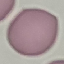
result: negative for malaria parasites
preparation: thin blood film
stain: Giemsa
capture: smartphone through the microscope eyepiece
image_type: cell patch, automatically extracted from a larger field of view and resized to 64 × 64 pixels